Locate and identify every blood parasite.
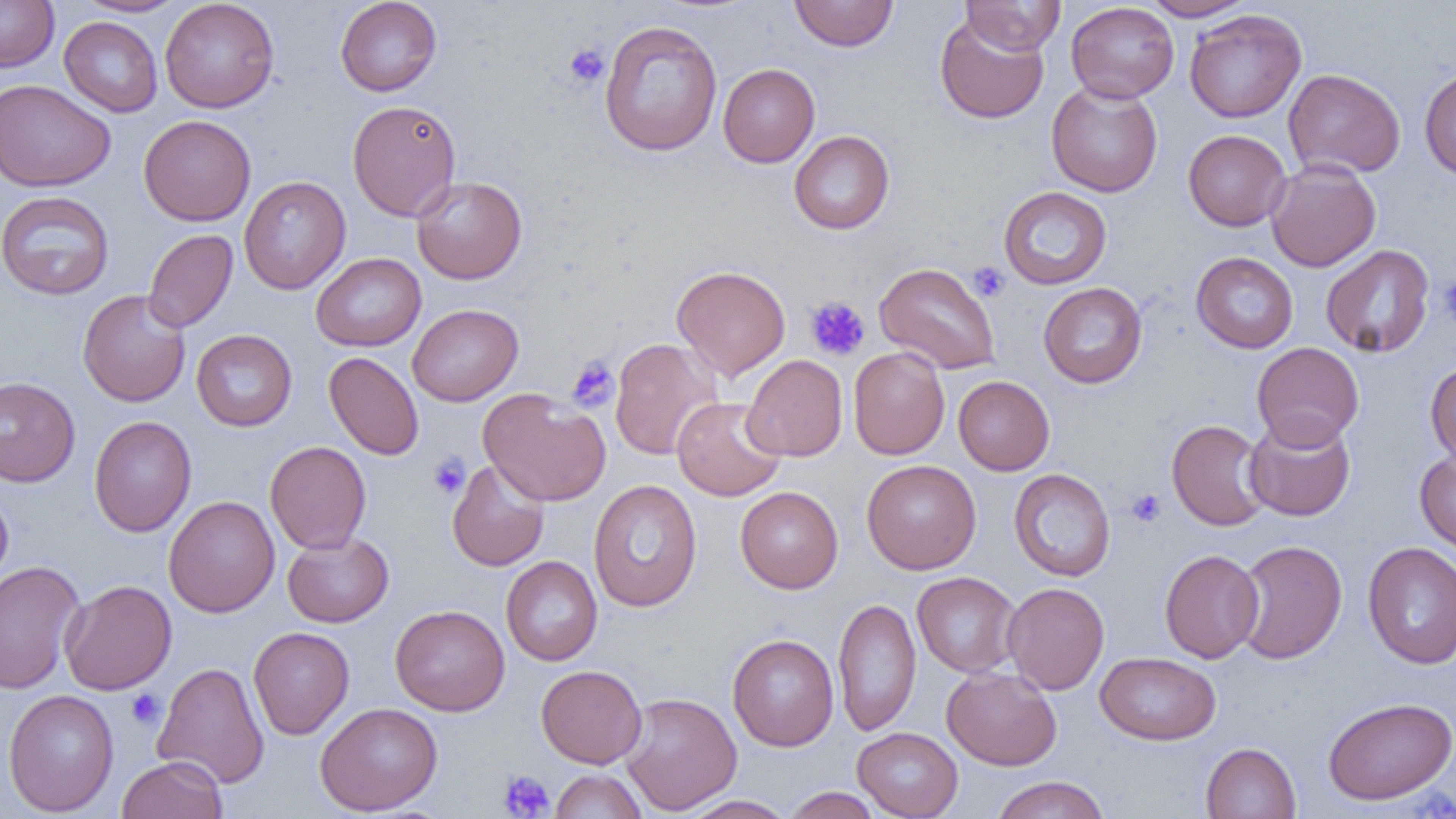
No blood parasites observed.

Approximate bounding boxes as (x1, y1, x2, y2) in pixels. Platelet locations: (564, 43, 609, 88), (968, 262, 1009, 302), (1436, 275, 1456, 328), (805, 296, 870, 361), (566, 356, 619, 412), (428, 453, 470, 500), (1125, 488, 1166, 528), (125, 689, 165, 729), (498, 770, 555, 818). Uninfected red blood cell locations: (0, 0, 59, 72), (74, 0, 189, 17), (160, 0, 279, 113), (335, 0, 442, 96), (789, 0, 899, 52), (960, 0, 1065, 55), (1139, 0, 1255, 21), (1065, 2, 1179, 103), (1184, 9, 1306, 123), (935, 15, 1049, 125), (59, 16, 163, 116), (598, 20, 723, 157), (718, 63, 820, 167), (1419, 67, 1456, 180), (1283, 68, 1406, 179), (0, 79, 116, 192), (1046, 81, 1163, 197), (347, 99, 461, 221), (139, 115, 256, 226), (1183, 129, 1291, 231), (789, 130, 894, 234), (1265, 159, 1381, 272), (239, 175, 351, 294), (411, 176, 527, 284), (998, 186, 1112, 290), (0, 190, 115, 300), (143, 229, 238, 333), (1320, 244, 1435, 357), (1191, 252, 1298, 353), (310, 253, 426, 351), (875, 262, 1000, 374), (671, 265, 791, 380), (1038, 282, 1147, 388), (77, 289, 191, 407), (407, 304, 523, 406), (191, 329, 297, 431), (610, 338, 723, 461), (1252, 342, 1364, 450), (848, 346, 950, 460), (323, 352, 424, 460), (742, 354, 847, 461), (1425, 360, 1456, 467), (953, 375, 1054, 475), (0, 376, 80, 487), (479, 389, 610, 506), (672, 396, 786, 501), (1244, 414, 1356, 521), (89, 415, 196, 537), (1166, 419, 1271, 531), (265, 440, 371, 553), (1415, 450, 1456, 558), (446, 460, 550, 572), (862, 460, 981, 574), (1009, 468, 1115, 581), (588, 480, 702, 612), (735, 486, 843, 593), (0, 488, 13, 588), (163, 495, 280, 618), (282, 531, 394, 627), (1234, 539, 1347, 664), (1362, 542, 1456, 670), (1159, 549, 1265, 663), (501, 556, 602, 666), (0, 561, 86, 694), (912, 571, 1021, 678), (59, 579, 176, 695), (1002, 582, 1109, 695), (832, 597, 922, 736), (390, 604, 510, 716), (248, 626, 354, 739), (727, 633, 839, 751), (1094, 651, 1221, 745), (152, 661, 269, 789), (536, 664, 647, 768), (942, 666, 1062, 770), (3, 689, 119, 816), (619, 692, 742, 815), (1323, 696, 1456, 805), (315, 702, 443, 815), (852, 727, 964, 818), (1200, 742, 1300, 819), (117, 755, 227, 819), (550, 769, 647, 819), (989, 776, 1110, 819), (782, 787, 883, 818), (677, 795, 796, 818). Slide-level diagnosis: negative for blood parasites. Image is 1456×819 pixels. Captured at 1000x magnification. One field of a larger specimen. Thin blood smear. Optical microscopy.